Locate and identify every blood parasite.
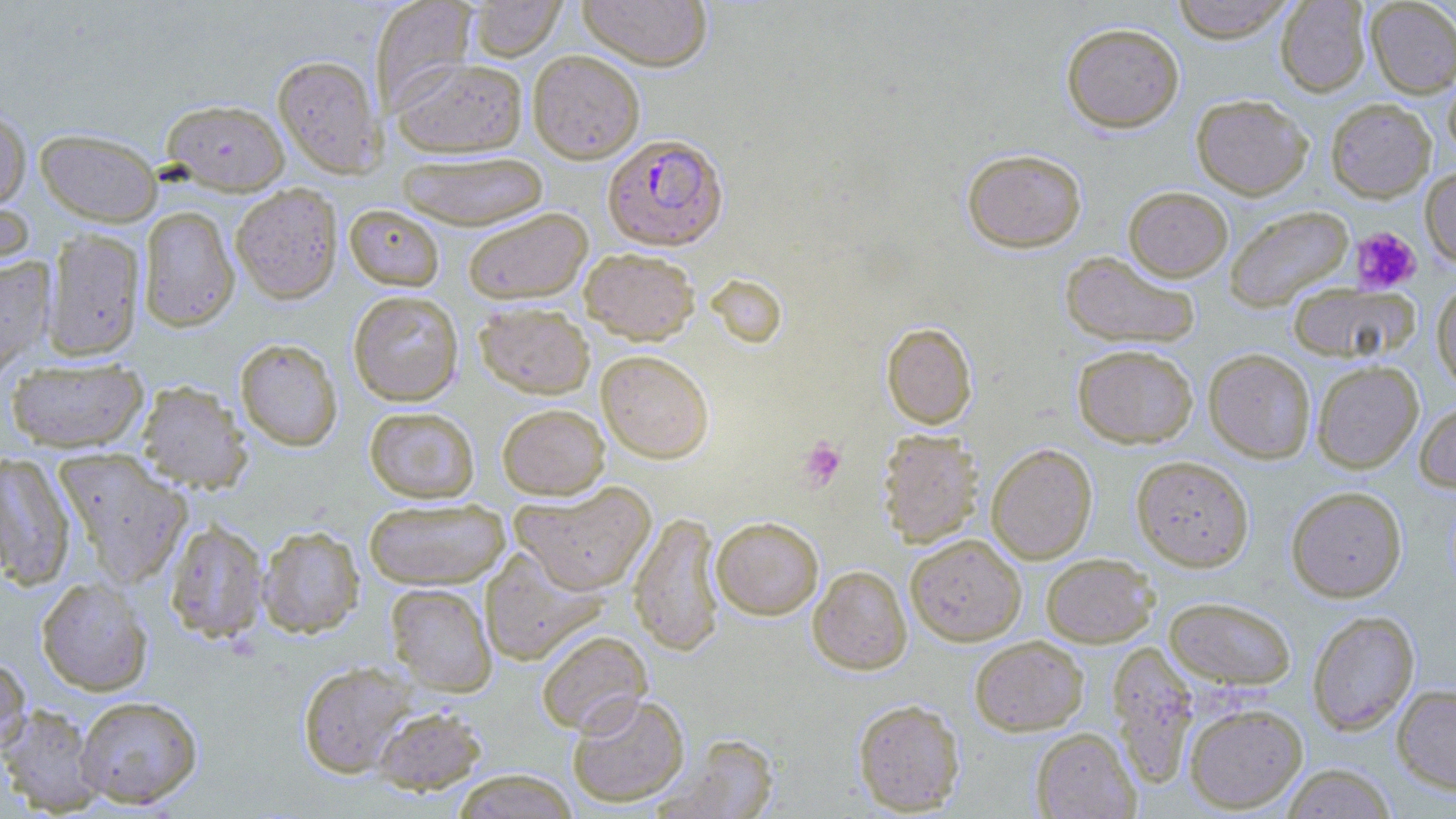
Approximate bounding boxes as [x1, y1, x2, y2] in pixels.
Plasmodium falciparum-infected red blood cells: [602, 133, 728, 251].
No Plasmodium ovale, Plasmodium malariae, Plasmodium vivax, Babesia divergens, or Trypanosoma brucei observed.

Platelet locations: [1351, 227, 1421, 293], [799, 436, 846, 489]. Uninfected red blood cell locations: [468, 0, 567, 61], [577, 0, 713, 70], [1169, 0, 1296, 43], [1275, 0, 1371, 97], [1365, 0, 1456, 98], [370, 1, 478, 113], [1061, 22, 1185, 133], [528, 50, 645, 163], [273, 54, 384, 177], [391, 57, 528, 157], [1443, 67, 1456, 164], [1191, 94, 1313, 199], [1326, 98, 1436, 202], [161, 99, 290, 195], [0, 107, 31, 212], [35, 128, 163, 226], [961, 148, 1087, 252], [396, 150, 550, 229], [1420, 167, 1456, 268], [231, 183, 343, 304], [1124, 186, 1233, 281], [0, 188, 35, 279], [344, 204, 445, 291], [1224, 205, 1354, 312], [138, 206, 240, 331], [462, 207, 592, 304], [43, 229, 145, 362], [580, 248, 700, 344], [1060, 250, 1200, 349], [0, 256, 55, 381], [1431, 280, 1456, 392], [1287, 282, 1418, 363], [348, 290, 464, 406], [475, 301, 595, 398], [881, 322, 977, 429], [235, 338, 343, 452], [1072, 344, 1199, 448], [1203, 348, 1316, 463], [596, 349, 714, 463], [5, 358, 148, 453], [1311, 360, 1423, 473], [136, 380, 252, 492], [1414, 399, 1456, 493], [497, 403, 609, 499], [364, 406, 479, 503], [877, 430, 985, 548], [986, 443, 1097, 563], [53, 449, 192, 587], [0, 452, 76, 591], [1131, 454, 1254, 571], [511, 482, 656, 595], [1286, 485, 1407, 602], [364, 498, 510, 590], [629, 511, 724, 657], [711, 516, 824, 620], [165, 520, 270, 643], [257, 525, 365, 638], [906, 534, 1026, 645], [480, 546, 609, 665], [1041, 553, 1158, 647], [808, 565, 912, 675], [36, 577, 153, 695], [386, 583, 497, 695], [1164, 595, 1297, 690], [1307, 610, 1420, 736], [536, 630, 653, 735], [970, 635, 1088, 735], [1107, 641, 1198, 788], [0, 655, 31, 755], [298, 661, 418, 778], [1392, 684, 1456, 794], [567, 692, 690, 808], [75, 695, 203, 808], [853, 699, 965, 814], [1184, 702, 1308, 812], [0, 704, 105, 815], [371, 704, 487, 794], [1031, 727, 1139, 818], [657, 733, 781, 818], [1279, 763, 1397, 818], [452, 770, 579, 818]. Slide-level diagnosis: Plasmodium falciparum. Single field of view. Light microscopy. May-Grünwald-Giemsa stain. Thin blood film. Image is 1456×819 pixels. 1000x magnification.